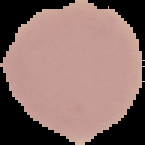
result: no malaria parasites detected
image_size: 145×145 pixels
preparation: thin blood smear
image_type: cell region segmented out of the field of view; surrounding area masked to black